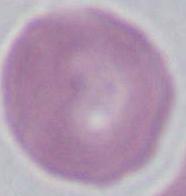

A red blood cell is seen. Micrograph. 1000x magnification.